Name the cell type shown.
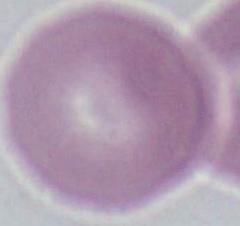
This is an erythrocyte.

Captured at 1000x magnification. Micrograph.